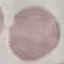

Summary:
  - Result: no malaria parasites detected
  - Preparation: thin blood film
  - Image type: automatically extracted cell patch, resized to 64 × 64 pixels
  - Stain: Giemsa
  - Capture: smartphone through the microscope eyepiece